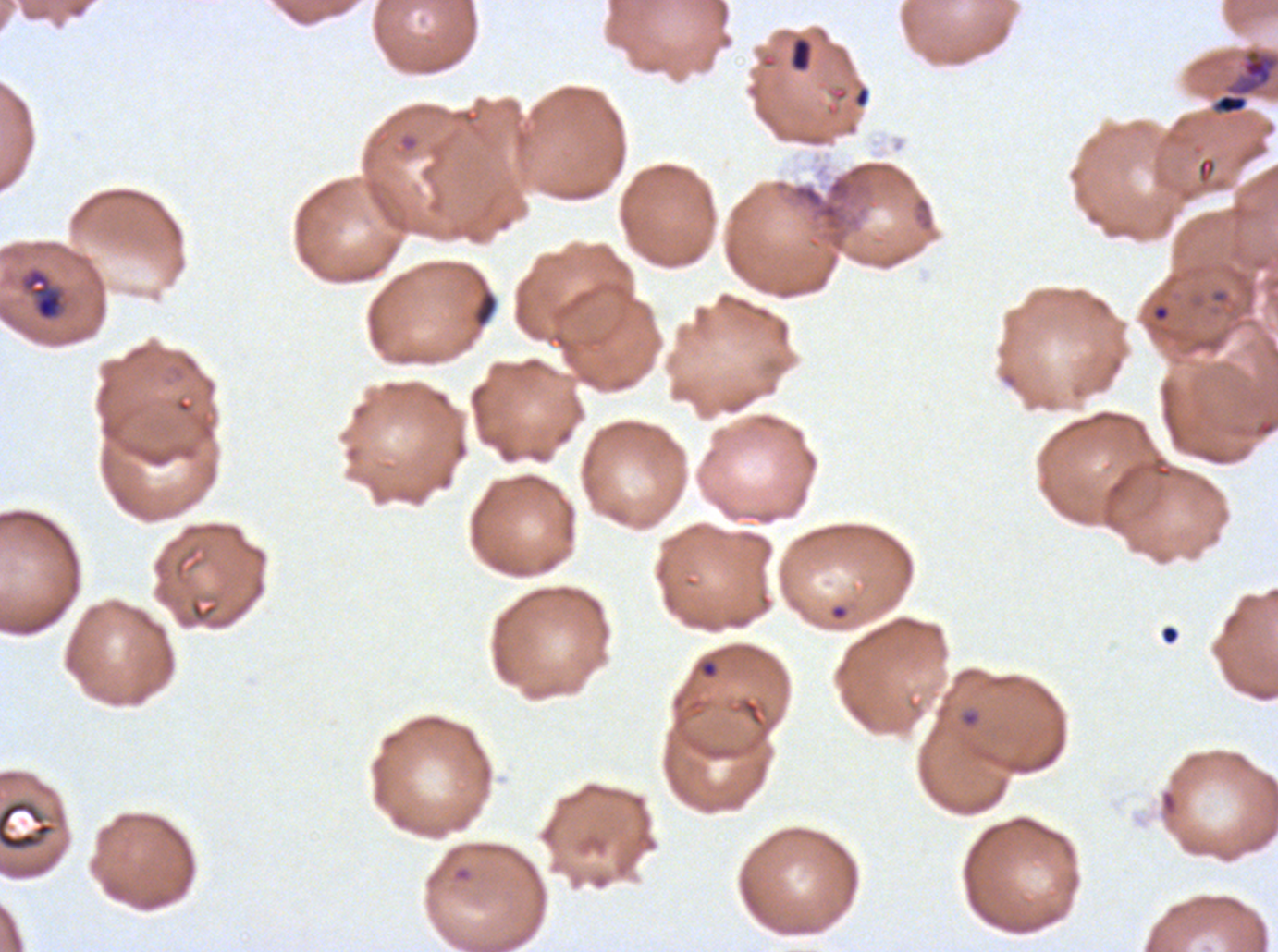
notation = approximate bounding boxes as [x1, y1, x2, y2] in pixels
ring locations = [961, 711, 979, 726]
late-ring/early-trophozoite locations = [19, 266, 66, 322]
debris locations = [790, 37, 812, 71], [473, 289, 498, 327], [0, 799, 55, 851]
late trophozoite locations = [1210, 47, 1277, 116]
image size = 1278×952 pixels
specimen = Plasmodium falciparum from a patient in The Gambia, cultured ex vivo for 24 to 48 hours
life-cycle stages observed = ring, late-ring/early-trophozoite, late trophozoite
field of view = sub-image separated from a larger composite
stain = Giemsa
preparation = thin blood film